State which parasite is depicted.
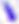

Toxoplasma gondii.

Summary:
  - Modality: micrograph
  - Magnification: 400x